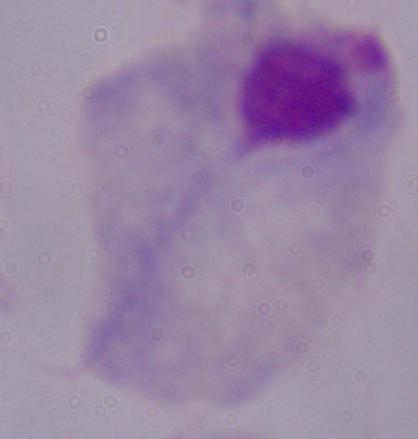
modality: micrograph
identification: trichomonad
magnification: 1000x